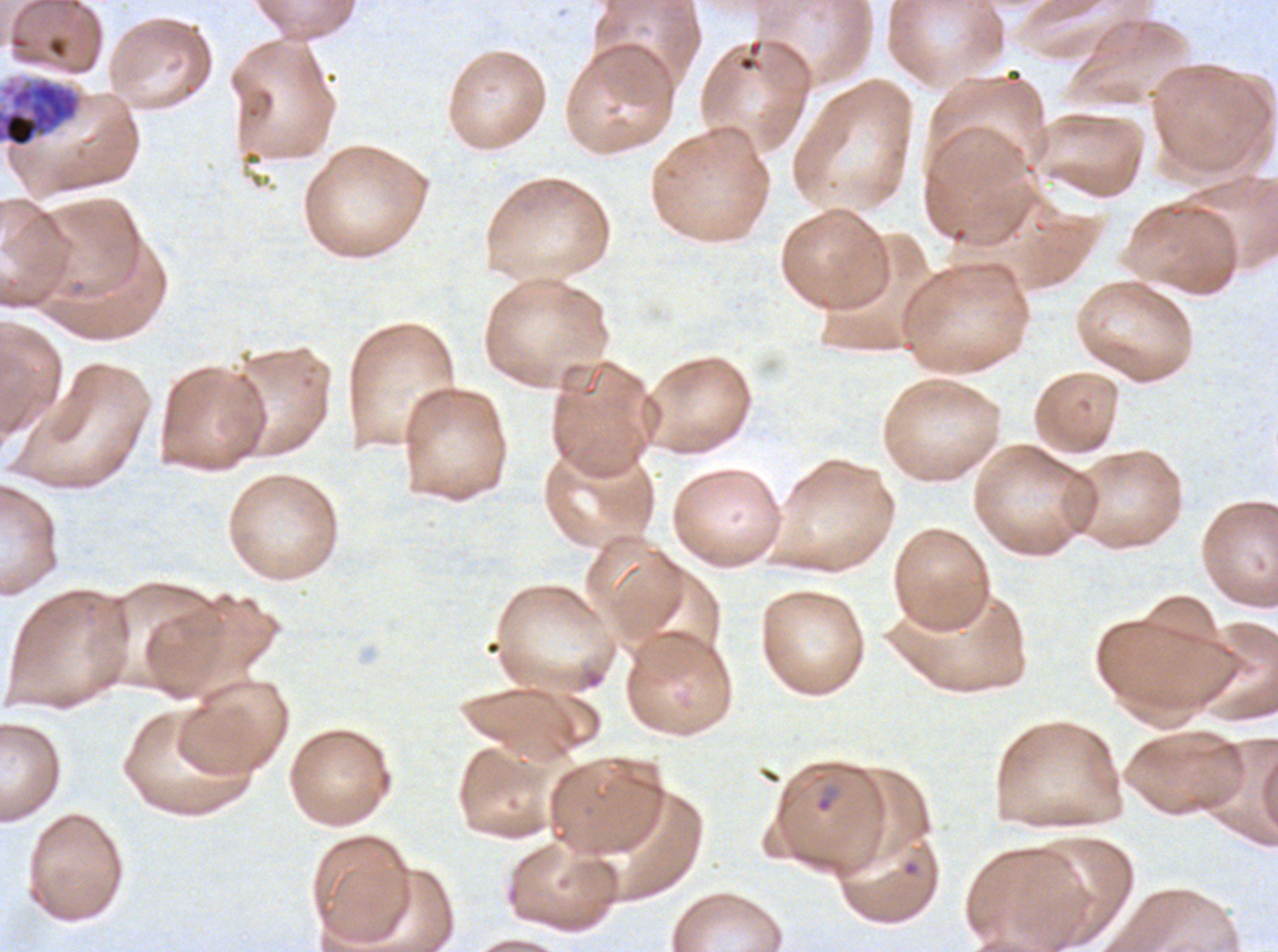
Approximate bounding boxes as (x1, y1, x2, y2) in pixels.
Summary:
  - Early schizont locations: (0, 75, 84, 149)
  - Ring locations: (814, 784, 840, 814)
  - Stain: Giemsa
  - Image size: 1278×952 pixels
  - Specimen: Plasmodium falciparum cultured ex vivo for 24 to 48 hours, from a patient in The Gambia
  - Preparation: thin blood film
  - Life-cycle stages observed: ring, early schizont
  - Field of view: one sub-image of a larger composite